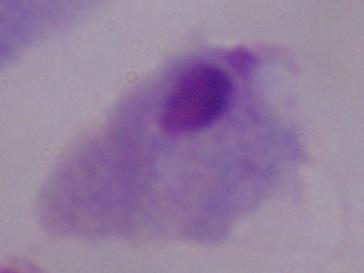
Captured at 1000x magnification. A trichomonad is shown. Photomicrograph.